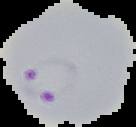

result = malaria parasites identified
preparation = thin blood smear
image type = cell region segmented out of the field of view; surrounding area masked to black
image size = 136×127 pixels